Give the extent of all Plasmodium falciparum-infected red blood cells.
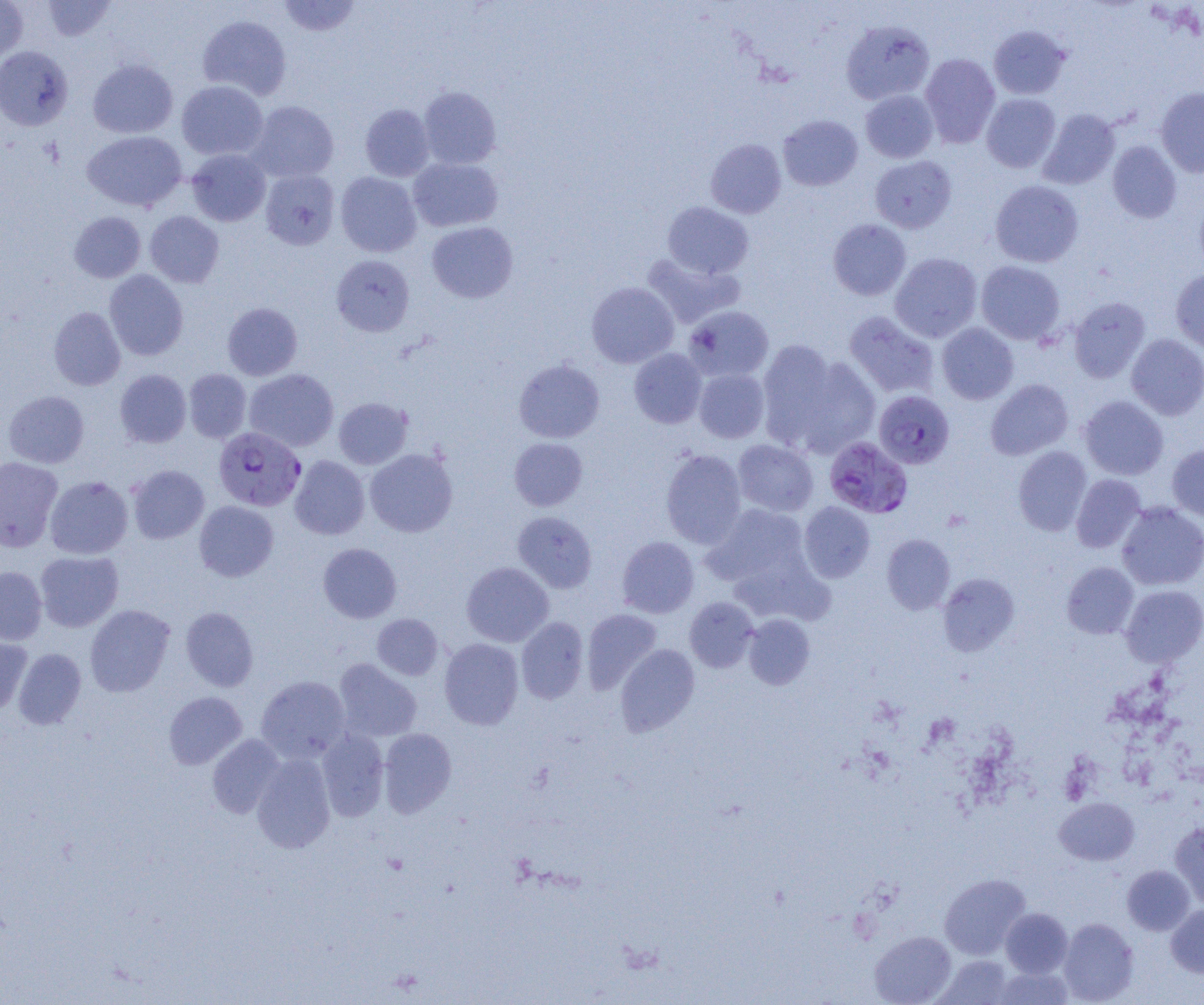
Approximate bounding boxes as (x1, y1, x2, y2) in pixels.
Plasmodium falciparum-infected red blood cells: (874, 390, 954, 469), (213, 427, 306, 511), (824, 436, 912, 518).

{
  "slide_level_diagnosis": "Plasmodium falciparum",
  "image_size": "1204×1005 pixels",
  "magnification": "1000x",
  "field_of_view": "single",
  "modality": "optical microscopy",
  "uninfected_red_blood_cell_locations": "approximate bounding boxes as (x1, y1, x2, y2) in pixels: (0, 0, 28, 62), (42, 0, 116, 41), (278, 0, 362, 37), (198, 15, 292, 100), (841, 19, 935, 104), (988, 25, 1071, 100), (0, 46, 73, 130), (920, 54, 1000, 147), (88, 59, 177, 138), (176, 80, 268, 160), (418, 86, 501, 169), (1155, 88, 1204, 177), (860, 90, 939, 163), (981, 94, 1061, 173), (247, 101, 339, 183), (360, 104, 435, 181), (1038, 109, 1120, 190), (778, 114, 863, 190), (82, 131, 187, 212), (706, 139, 786, 218), (1107, 141, 1181, 223), (187, 149, 271, 226), (869, 155, 957, 233), (408, 157, 502, 232), (261, 169, 340, 250), (335, 172, 422, 257), (990, 180, 1084, 267), (1194, 194, 1204, 274), (662, 202, 753, 279), (69, 211, 146, 283), (145, 211, 224, 287), (828, 218, 911, 300), (427, 222, 518, 303), (890, 252, 982, 342), (642, 254, 743, 328), (331, 255, 415, 337), (976, 261, 1065, 344), (1171, 269, 1204, 352), (104, 270, 188, 360), (586, 282, 679, 368), (1069, 297, 1150, 383), (222, 302, 303, 380), (683, 305, 774, 382), (49, 306, 125, 391), (843, 311, 939, 398), (937, 323, 1018, 404), (1125, 333, 1204, 420), (758, 339, 841, 450), (629, 348, 707, 428), (785, 353, 882, 459), (514, 359, 605, 443), (694, 368, 769, 443), (115, 369, 191, 447), (184, 369, 252, 443), (244, 369, 339, 452), (985, 379, 1073, 460), (3, 391, 89, 468), (1079, 396, 1169, 480), (333, 397, 413, 469), (509, 438, 588, 511), (733, 439, 818, 517), (1167, 445, 1204, 521), (1013, 446, 1092, 536), (365, 449, 458, 537), (660, 449, 746, 548), (290, 455, 370, 539), (0, 457, 63, 551), (127, 465, 209, 543), (1071, 474, 1146, 553), (45, 475, 132, 559), (194, 501, 279, 581), (799, 501, 875, 582), (1117, 502, 1204, 590), (705, 503, 809, 585), (512, 511, 597, 593), (882, 534, 955, 614), (617, 536, 699, 618), (318, 543, 401, 623), (34, 551, 123, 632), (461, 562, 554, 647), (1062, 562, 1138, 639), (0, 566, 47, 644), (937, 573, 1019, 656), (1121, 585, 1204, 666), (684, 597, 759, 672), (85, 604, 175, 697), (181, 606, 259, 691), (582, 608, 662, 693), (372, 614, 443, 680), (743, 614, 815, 689), (516, 617, 588, 703), (0, 635, 32, 715), (439, 638, 524, 729), (615, 644, 699, 736), (13, 648, 86, 729), (333, 658, 422, 742), (256, 676, 351, 763), (163, 691, 247, 769), (378, 728, 456, 817), (317, 730, 389, 821), (207, 734, 285, 818), (252, 753, 335, 853), (1055, 797, 1139, 865), (1170, 821, 1204, 909), (1122, 865, 1195, 935), (939, 873, 1031, 959), (1166, 904, 1204, 977), (1001, 908, 1072, 977), (1058, 918, 1139, 1004), (870, 931, 956, 1005), (934, 954, 1014, 1004), (994, 966, 1074, 1004)",
  "preparation": "thin blood film"
}